Identify the preparation type.
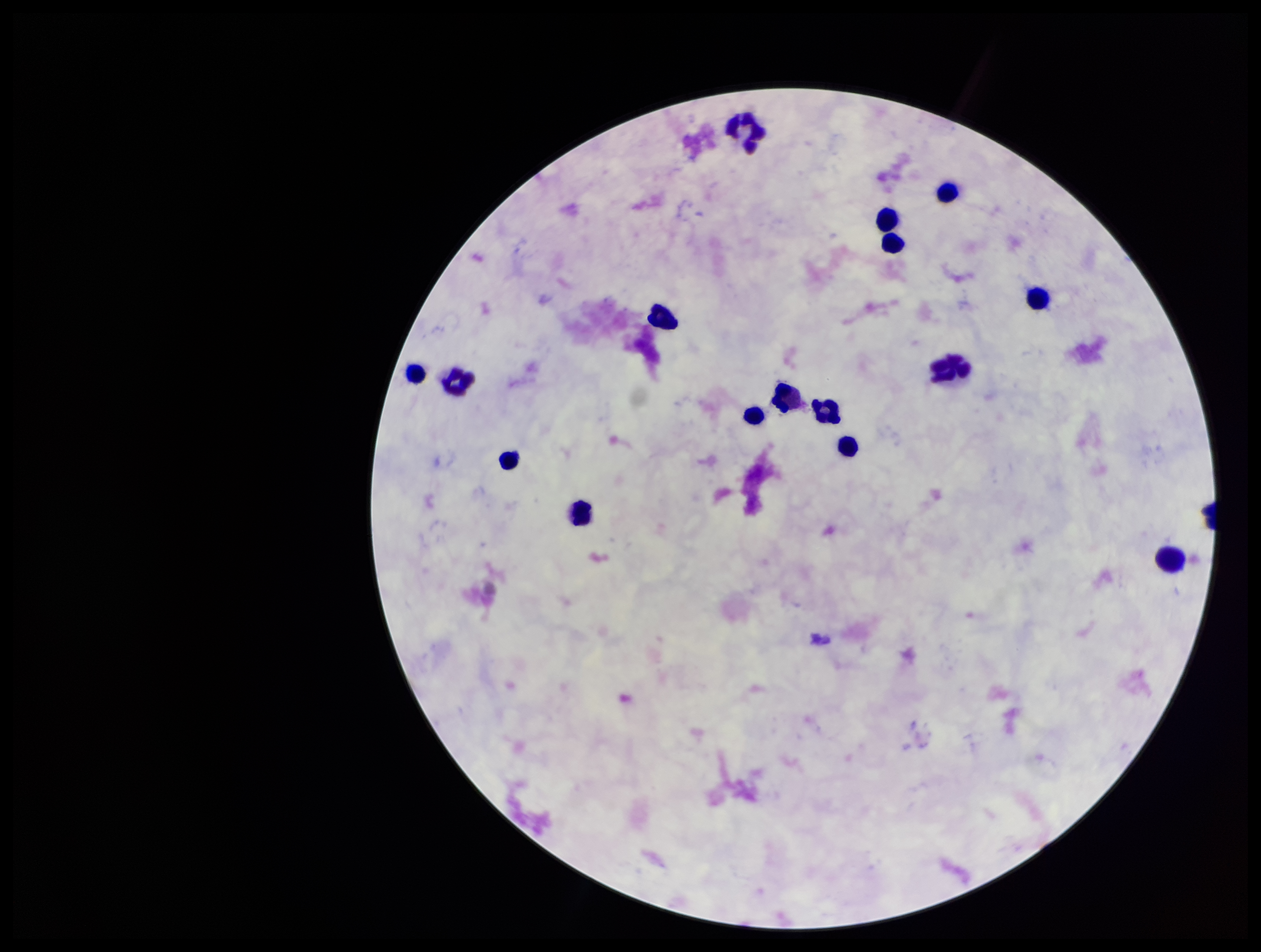

It is a thick blood smear.

Plasmodium parasites = none identified
stain = Giemsa
field of view = one from this slide
leukocyte count = 16
patient malaria status = negative
image size = 1261×952 pixels
capture = smartphone photograph through the microscope eyepiece
parasite count = 0